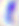
Summary:
  - Modality: photomicrograph
  - Identification: Toxoplasma gondii
  - Magnification: 400x